Report the malaria status of this cell.
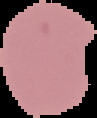
It is uninfected.

Cell region segmented out of the field of view; the surrounding area is masked to black. Image is 97×118 pixels. From a thin blood smear.